Identify the preparation type.
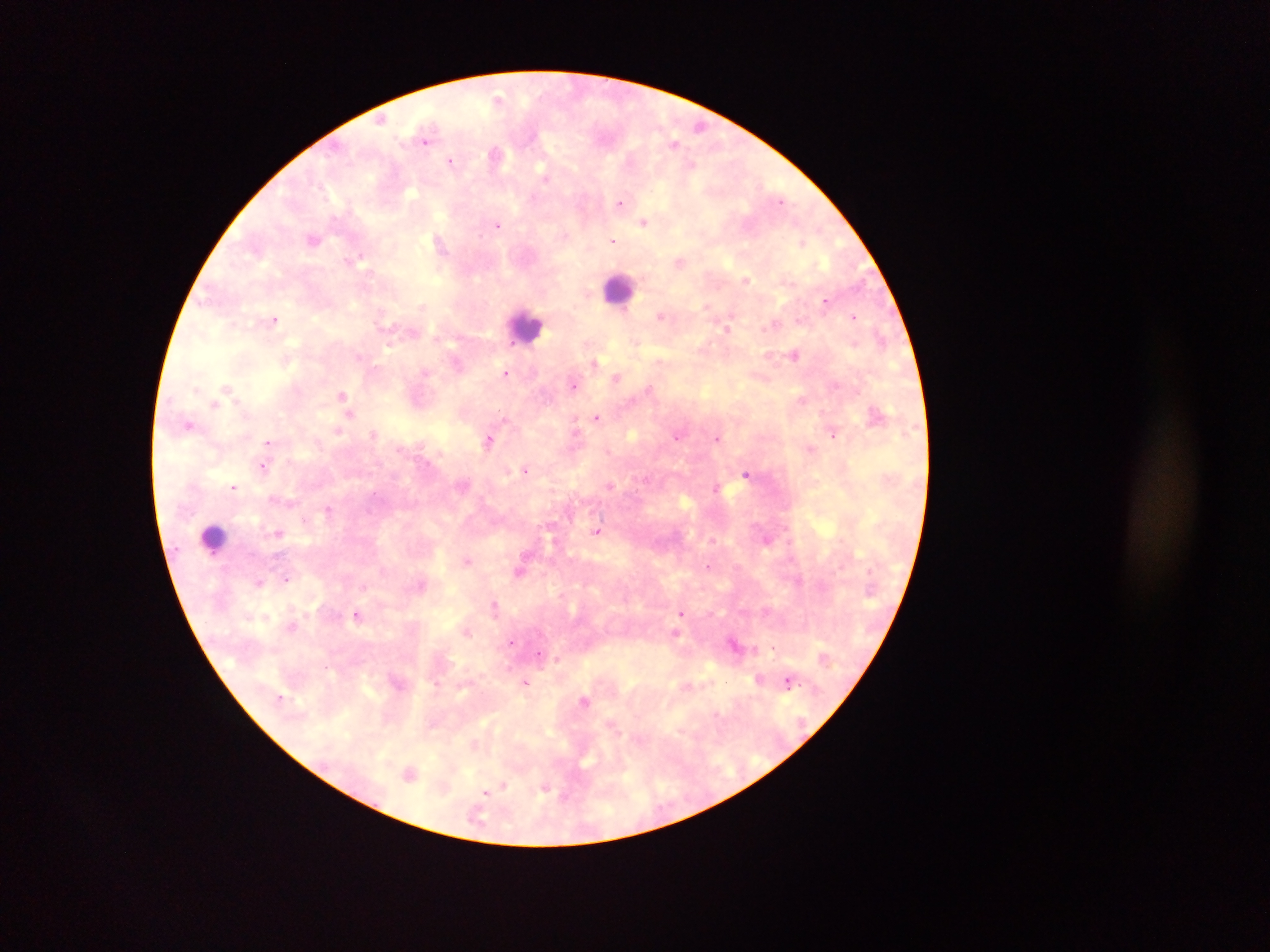
This is a thick smear.

Approximate centers as (x, y) in pixels. Malaria parasite locations: (498, 96), (380, 120), (675, 140), (426, 145), (495, 155), (451, 162), (620, 202), (645, 222), (498, 226), (613, 241), (803, 241), (441, 245), (348, 260), (747, 280), (826, 301), (423, 304), (707, 305), (731, 314), (660, 316), (854, 316), (274, 319), (774, 323), (794, 354), (361, 356), (660, 359), (594, 361), (506, 372), (617, 377), (573, 384), (228, 388), (650, 388), (343, 393), (803, 399), (213, 405), (350, 413), (874, 413), (597, 417), (505, 419), (575, 421), (188, 424), (338, 431), (576, 431), (374, 434), (833, 434), (677, 436), (719, 438), (267, 442), (488, 443), (810, 449), (265, 466), (526, 470), (746, 472), (610, 485), (233, 487), (717, 487), (328, 510), (550, 532), (597, 532), (279, 533), (766, 540), (466, 560), (708, 565), (520, 572), (286, 576), (259, 583), (420, 585), (494, 604), (681, 613), (358, 615), (468, 631), (676, 633), (512, 642), (734, 642), (558, 660), (328, 667), (759, 678), (788, 680), (527, 683), (688, 685), (584, 700), (473, 745), (409, 770), (504, 786), (546, 788), (502, 790), (487, 793). Leukocyte locations: (621, 290), (523, 324), (208, 538). Single field of view. Collected in Ghana. Mobile-phone photograph taken through the microscope. Image is 1270×952 pixels.